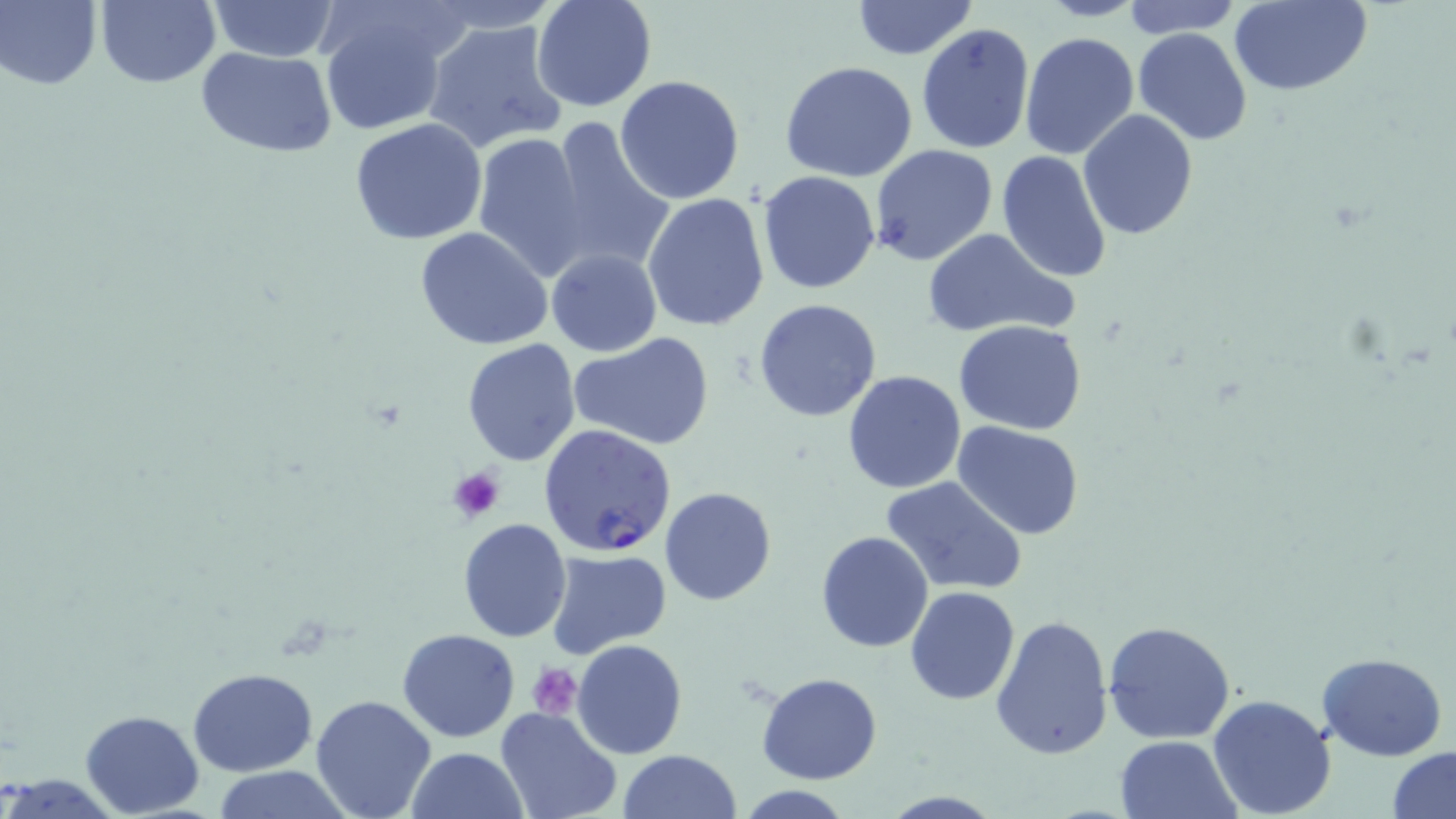

Approximate bounding boxes as named x1/y1/x2/y2 corners in pixels. Platelet locations: (x1=447, y1=464, x2=507, y2=522), (x1=526, y1=663, x2=581, y2=719). Plasmodium falciparum-infected red blood cell locations: (x1=539, y1=424, x2=678, y2=558). Uninfected red blood cell locations: (x1=1, y1=0, x2=102, y2=90), (x1=95, y1=0, x2=220, y2=88), (x1=206, y1=0, x2=342, y2=60), (x1=530, y1=0, x2=658, y2=114), (x1=1038, y1=0, x2=1148, y2=21), (x1=1122, y1=0, x2=1241, y2=37), (x1=1228, y1=0, x2=1371, y2=97), (x1=849, y1=1, x2=979, y2=58), (x1=319, y1=9, x2=453, y2=138), (x1=424, y1=17, x2=567, y2=154), (x1=917, y1=24, x2=1034, y2=154), (x1=1133, y1=28, x2=1254, y2=147), (x1=1020, y1=32, x2=1138, y2=159), (x1=195, y1=47, x2=339, y2=160), (x1=780, y1=61, x2=920, y2=183), (x1=615, y1=76, x2=745, y2=205), (x1=1077, y1=110, x2=1199, y2=243), (x1=350, y1=118, x2=489, y2=246), (x1=547, y1=119, x2=676, y2=276), (x1=470, y1=128, x2=592, y2=280), (x1=869, y1=144, x2=997, y2=266), (x1=995, y1=149, x2=1111, y2=285), (x1=757, y1=170, x2=883, y2=294), (x1=641, y1=192, x2=770, y2=331), (x1=415, y1=226, x2=552, y2=351), (x1=921, y1=229, x2=1078, y2=340), (x1=545, y1=248, x2=662, y2=356), (x1=754, y1=299, x2=883, y2=423), (x1=954, y1=319, x2=1086, y2=436), (x1=569, y1=331, x2=716, y2=451), (x1=461, y1=338, x2=580, y2=465), (x1=842, y1=371, x2=967, y2=494), (x1=951, y1=418, x2=1087, y2=540), (x1=879, y1=476, x2=1026, y2=597), (x1=659, y1=486, x2=776, y2=605), (x1=457, y1=519, x2=572, y2=642), (x1=815, y1=530, x2=933, y2=652), (x1=546, y1=549, x2=671, y2=656), (x1=906, y1=585, x2=1021, y2=706), (x1=989, y1=613, x2=1114, y2=761), (x1=1102, y1=619, x2=1235, y2=744), (x1=396, y1=628, x2=520, y2=743), (x1=572, y1=638, x2=688, y2=758), (x1=1317, y1=651, x2=1448, y2=760), (x1=187, y1=667, x2=318, y2=776), (x1=757, y1=673, x2=882, y2=786), (x1=310, y1=695, x2=437, y2=819), (x1=1207, y1=695, x2=1336, y2=818), (x1=496, y1=708, x2=621, y2=819), (x1=79, y1=710, x2=204, y2=818), (x1=1115, y1=735, x2=1240, y2=819), (x1=1387, y1=746, x2=1456, y2=819), (x1=406, y1=747, x2=528, y2=819), (x1=617, y1=750, x2=741, y2=819), (x1=205, y1=767, x2=356, y2=819). Slide-level diagnosis: Plasmodium falciparum. 1000x magnification. May-Grünwald-Giemsa-stained preparation. Thin blood smear. Single field of view. Light microscopy. Image is 1456×819 pixels.